Assess this cell for malaria.
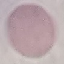

It is uninfected.

Summary:
  - Preparation: thin smear
  - Capture: smartphone through the microscope eyepiece
  - Stain: Giemsa
  - Image type: automatically extracted cell patch, resized to 64 × 64 pixels